Name the parasite shown.
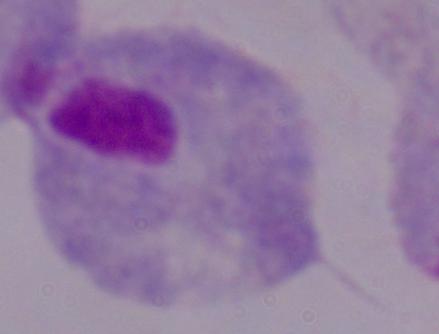

This is a trichomonad.

Micrograph. Captured at 1000x magnification.